Name the cell type shown.
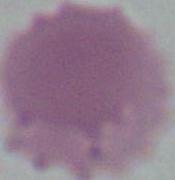
This is an erythrocyte.

Summary:
  - Modality: micrograph
  - Magnification: 1000x